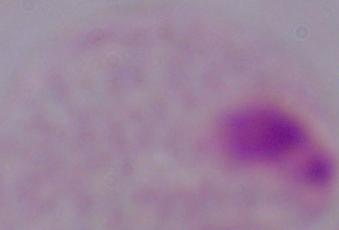
modality = micrograph
identification = trichomonad
magnification = 1000x